Assess for malaria.
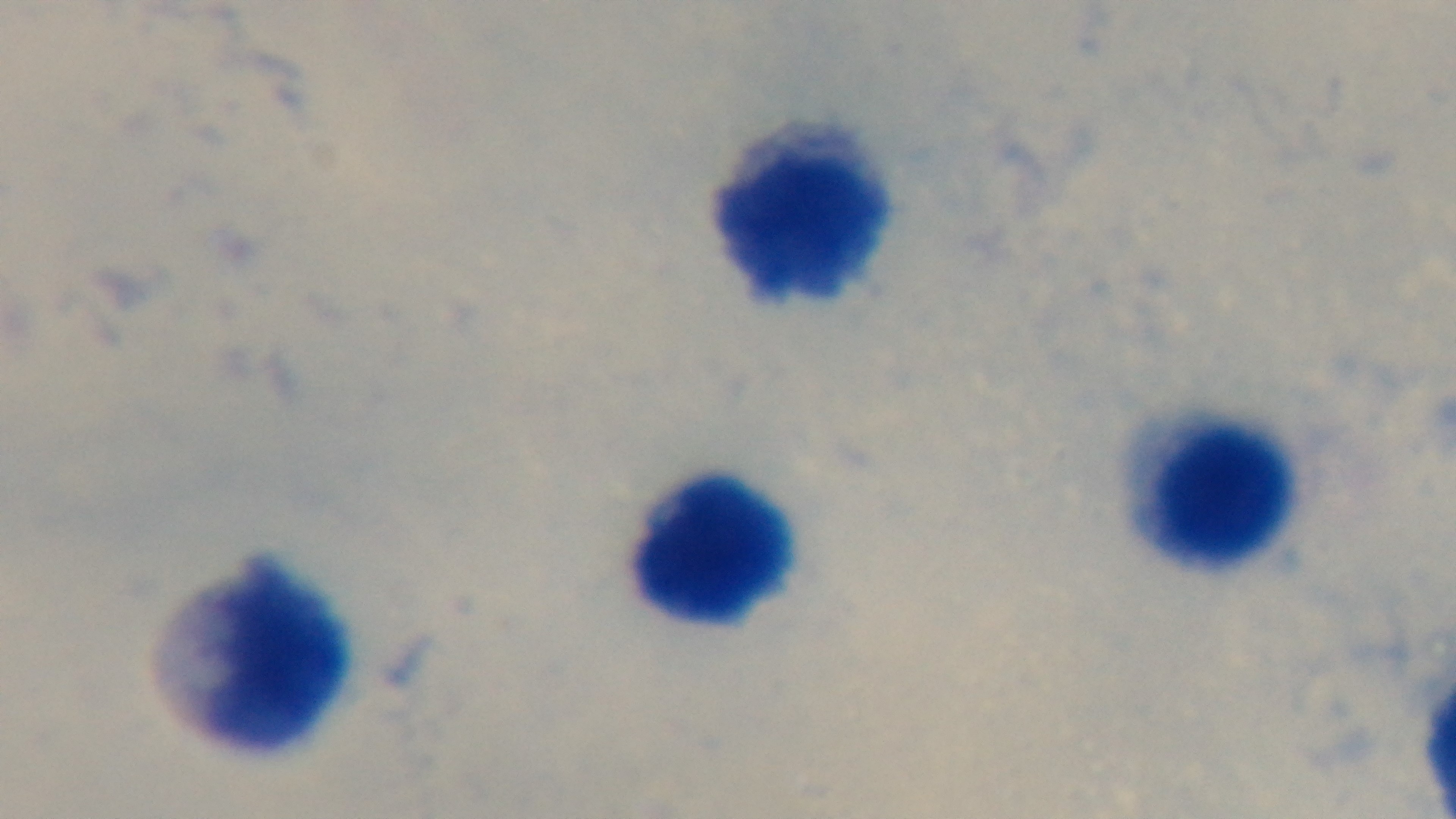

It is uninfected.

Summary:
  - Objective: 100x oil immersion
  - Field of view: one from the slide
  - Modality: light microscopy
  - Stain: Giemsa
  - Capture: mounted 4K digital camera
  - Preparation: thick